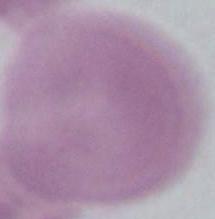

Photomicrograph. An erythrocyte is seen. Captured at 1000x magnification.